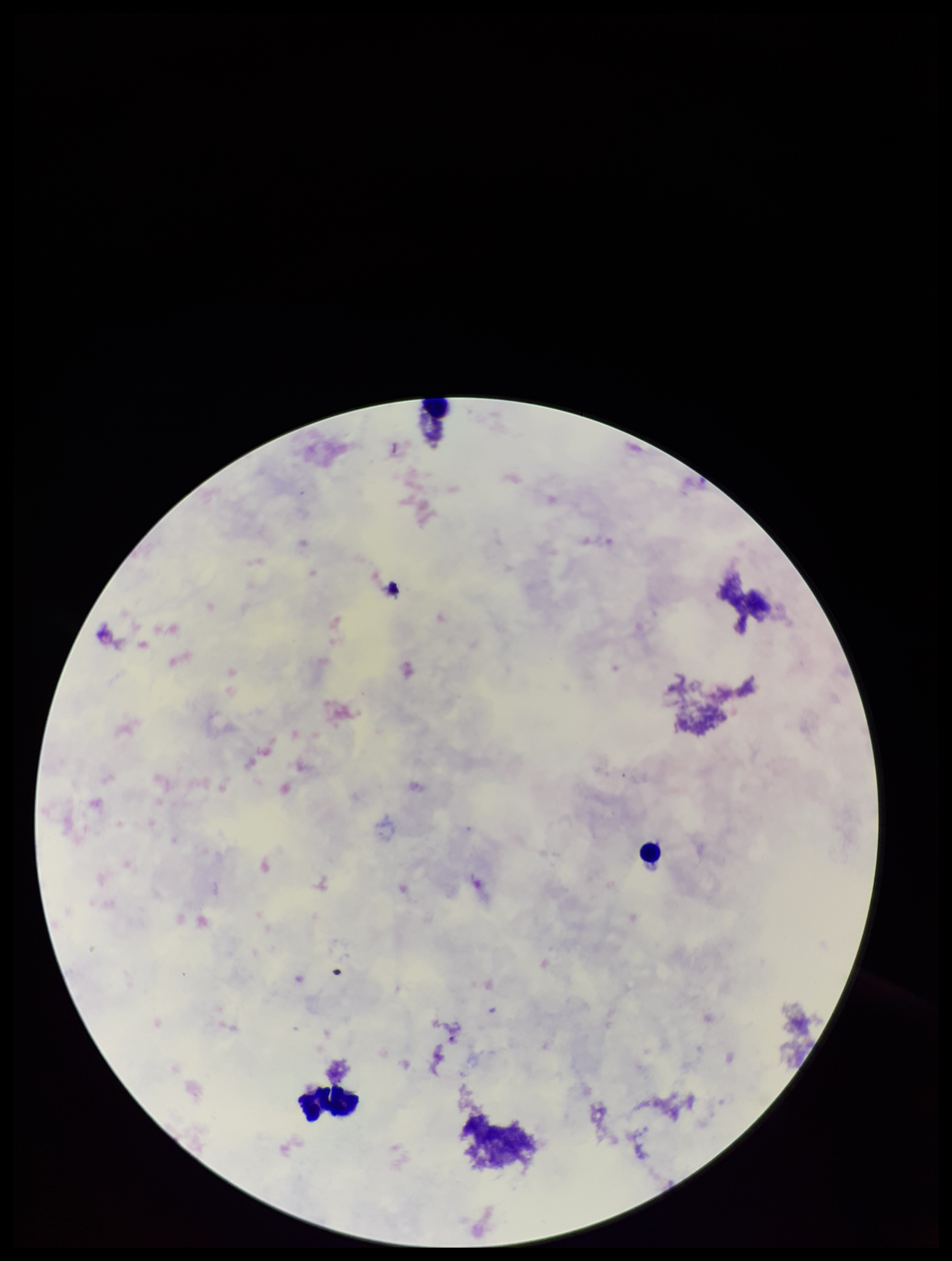
image size = 952×1261 pixels
stain = Giemsa
preparation = thick
patient malaria status = negative
parasite count = 0
Plasmodium parasites = none seen
field of view = one from this slide
capture = smartphone photograph through the microscope eyepiece
leukocyte count = 1